Report the malaria status of this cell.
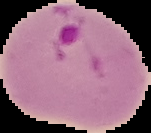

It is parasitized.

Segmented cell region on a black background. From a thin blood smear. Image is 151×133 pixels.